Comment on the morphology of the red blood cells.
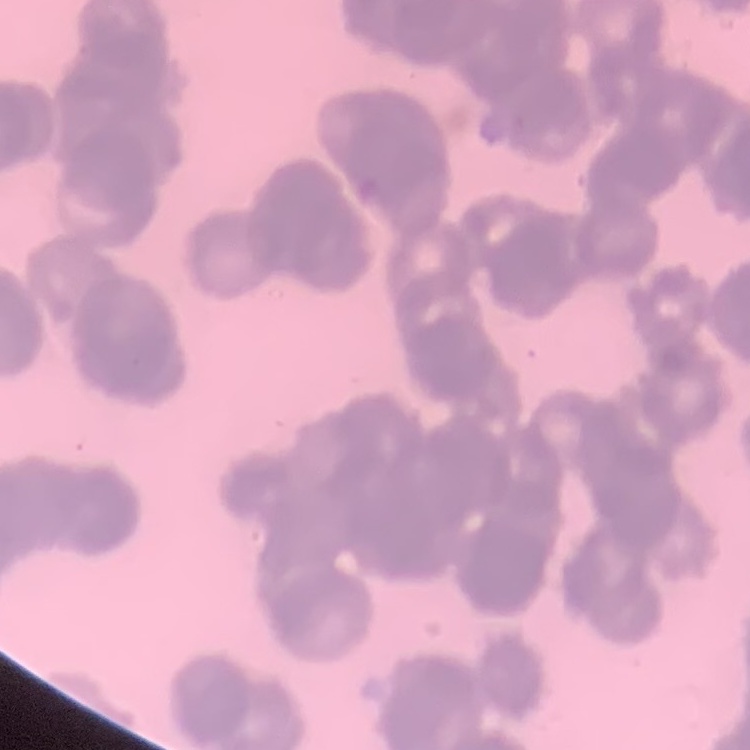

Rouleaux formation.

Thin peripheral smear. Square crop of a larger photomicrograph. Stained with either Field's or Giemsa.